Locate and identify every blood parasite.
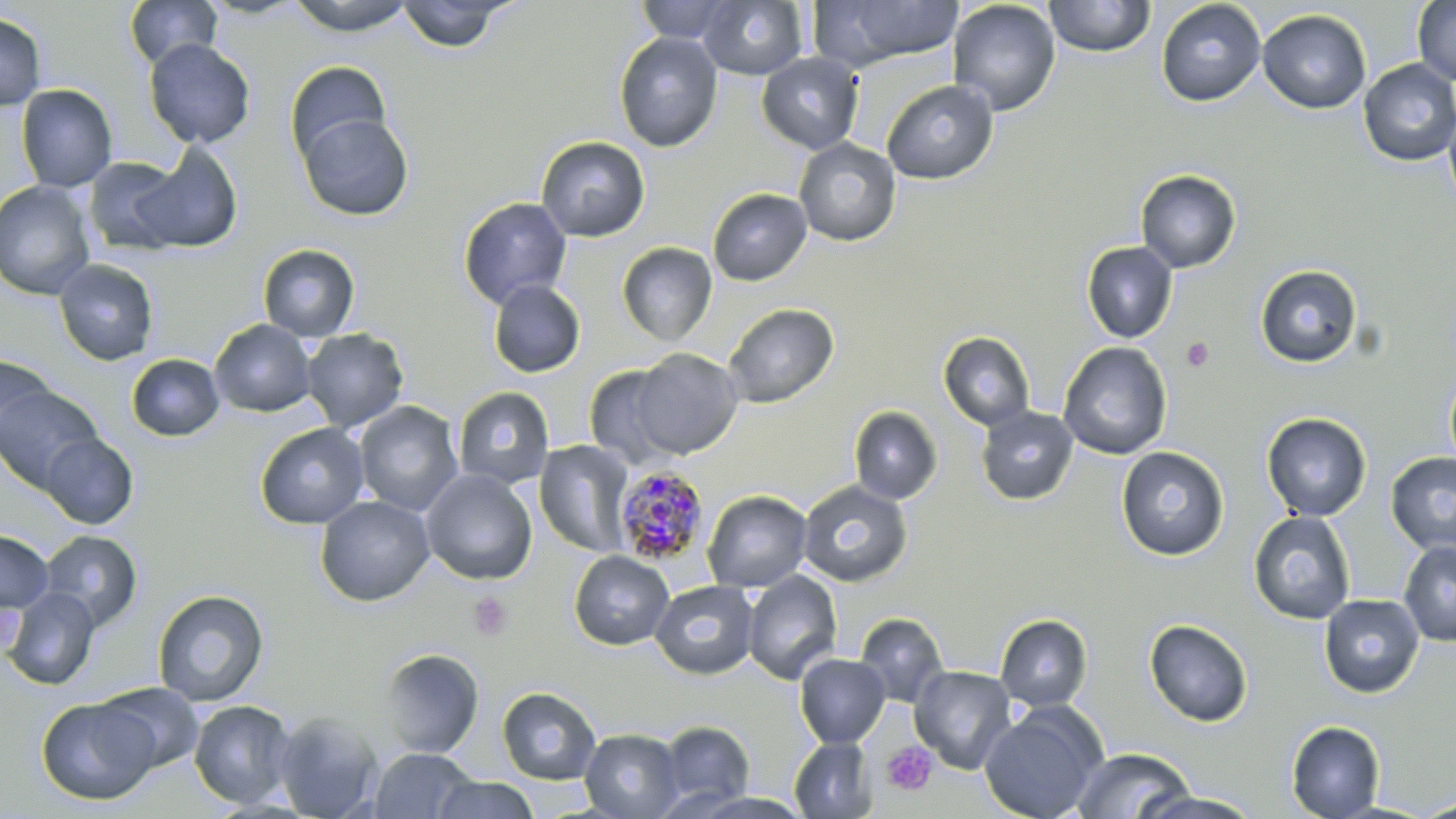

Approximate bounding boxes as named x1/y1/x2/y2 corners in pixels.
Plasmodium malariae-infected red blood cells: (x1=613, y1=466, x2=710, y2=564).
No Plasmodium falciparum, Plasmodium ovale, Plasmodium vivax, Babesia divergens, or Trypanosoma brucei observed.

Uninfected red blood cell locations: (x1=124, y1=0, x2=223, y2=70), (x1=286, y1=0, x2=416, y2=36), (x1=634, y1=0, x2=738, y2=43), (x1=697, y1=0, x2=808, y2=80), (x1=947, y1=0, x2=1062, y2=116), (x1=1044, y1=0, x2=1156, y2=58), (x1=1411, y1=0, x2=1456, y2=85), (x1=395, y1=1, x2=514, y2=53), (x1=812, y1=1, x2=965, y2=71), (x1=1155, y1=1, x2=1266, y2=107), (x1=1257, y1=9, x2=1372, y2=114), (x1=0, y1=13, x2=47, y2=110), (x1=613, y1=32, x2=723, y2=152), (x1=144, y1=38, x2=256, y2=149), (x1=756, y1=52, x2=864, y2=154), (x1=1358, y1=59, x2=1456, y2=167), (x1=285, y1=61, x2=392, y2=167), (x1=882, y1=79, x2=999, y2=185), (x1=16, y1=84, x2=118, y2=192), (x1=1443, y1=102, x2=1456, y2=216), (x1=297, y1=111, x2=414, y2=221), (x1=535, y1=135, x2=651, y2=242), (x1=793, y1=138, x2=902, y2=247), (x1=129, y1=143, x2=243, y2=254), (x1=83, y1=157, x2=187, y2=256), (x1=1135, y1=169, x2=1241, y2=273), (x1=0, y1=180, x2=97, y2=300), (x1=707, y1=188, x2=812, y2=287), (x1=457, y1=197, x2=572, y2=309), (x1=1081, y1=241, x2=1177, y2=343), (x1=617, y1=242, x2=717, y2=346), (x1=257, y1=244, x2=361, y2=342), (x1=53, y1=259, x2=158, y2=366), (x1=1255, y1=264, x2=1362, y2=367), (x1=487, y1=280, x2=586, y2=377), (x1=723, y1=303, x2=839, y2=408), (x1=210, y1=319, x2=316, y2=417), (x1=300, y1=328, x2=410, y2=432), (x1=938, y1=331, x2=1036, y2=430), (x1=1058, y1=342, x2=1172, y2=460), (x1=630, y1=348, x2=743, y2=459), (x1=0, y1=353, x2=58, y2=455), (x1=126, y1=354, x2=225, y2=442), (x1=583, y1=364, x2=683, y2=469), (x1=1445, y1=364, x2=1456, y2=478), (x1=0, y1=386, x2=104, y2=493), (x1=452, y1=386, x2=555, y2=490), (x1=354, y1=401, x2=463, y2=516), (x1=848, y1=405, x2=943, y2=504), (x1=975, y1=406, x2=1078, y2=505), (x1=1261, y1=412, x2=1372, y2=521), (x1=255, y1=423, x2=370, y2=529), (x1=39, y1=432, x2=139, y2=529), (x1=533, y1=440, x2=635, y2=558), (x1=1116, y1=446, x2=1229, y2=561), (x1=1385, y1=452, x2=1456, y2=555), (x1=420, y1=468, x2=538, y2=585), (x1=797, y1=480, x2=913, y2=587), (x1=702, y1=490, x2=813, y2=593), (x1=315, y1=495, x2=435, y2=607), (x1=1248, y1=511, x2=1357, y2=624), (x1=0, y1=529, x2=54, y2=615), (x1=38, y1=530, x2=143, y2=631), (x1=1398, y1=540, x2=1456, y2=647), (x1=568, y1=550, x2=674, y2=650), (x1=742, y1=570, x2=842, y2=684), (x1=650, y1=580, x2=759, y2=679), (x1=2, y1=588, x2=100, y2=690), (x1=152, y1=589, x2=269, y2=706), (x1=1319, y1=594, x2=1424, y2=697), (x1=854, y1=612, x2=950, y2=708), (x1=995, y1=614, x2=1093, y2=711), (x1=1144, y1=618, x2=1254, y2=727), (x1=378, y1=647, x2=484, y2=759), (x1=794, y1=653, x2=891, y2=747), (x1=909, y1=665, x2=1017, y2=773), (x1=94, y1=683, x2=204, y2=774), (x1=497, y1=686, x2=602, y2=784), (x1=35, y1=697, x2=160, y2=805), (x1=188, y1=700, x2=296, y2=808), (x1=979, y1=705, x2=1106, y2=819), (x1=272, y1=711, x2=384, y2=818), (x1=657, y1=720, x2=755, y2=809), (x1=1285, y1=720, x2=1385, y2=819), (x1=580, y1=728, x2=684, y2=819), (x1=789, y1=737, x2=878, y2=818), (x1=369, y1=747, x2=477, y2=819), (x1=1072, y1=747, x2=1196, y2=819), (x1=430, y1=776, x2=540, y2=819), (x1=1131, y1=791, x2=1266, y2=818), (x1=1410, y1=798, x2=1456, y2=818). Platelet locations: (x1=1181, y1=336, x2=1215, y2=371), (x1=468, y1=592, x2=513, y2=642), (x1=881, y1=742, x2=937, y2=795). Slide-level diagnosis: Plasmodium malariae. May-Grünwald-Giemsa stain. Thin blood film. Captured at 1000x magnification. Single field of view. Light microscopy. Image is 1456×819 pixels.